Comment on the morphology of the erythrocytes.
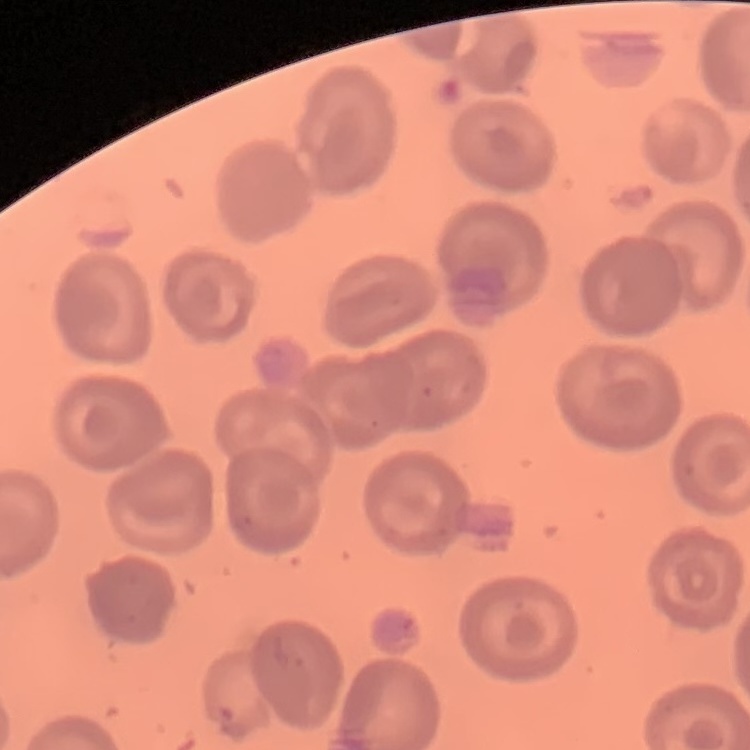

No rouleaux formation.

Summary:
  - Stain: Field's or Giemsa
  - Preparation: thin blood film
  - Image type: square crop of a larger photomicrograph